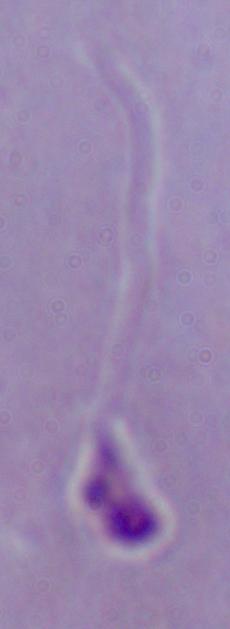
A Leishmania parasite is seen. Photomicrograph. 1000x magnification.